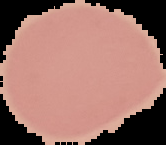

Image is 166×145 pixels. From a thin blood smear. Cell region segmented out of the field of view; the surrounding area is masked to black. Result: negative for malaria parasites.